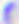

Toxoplasma gondii is shown. Micrograph. 400x magnification.